State the blood parasite species.
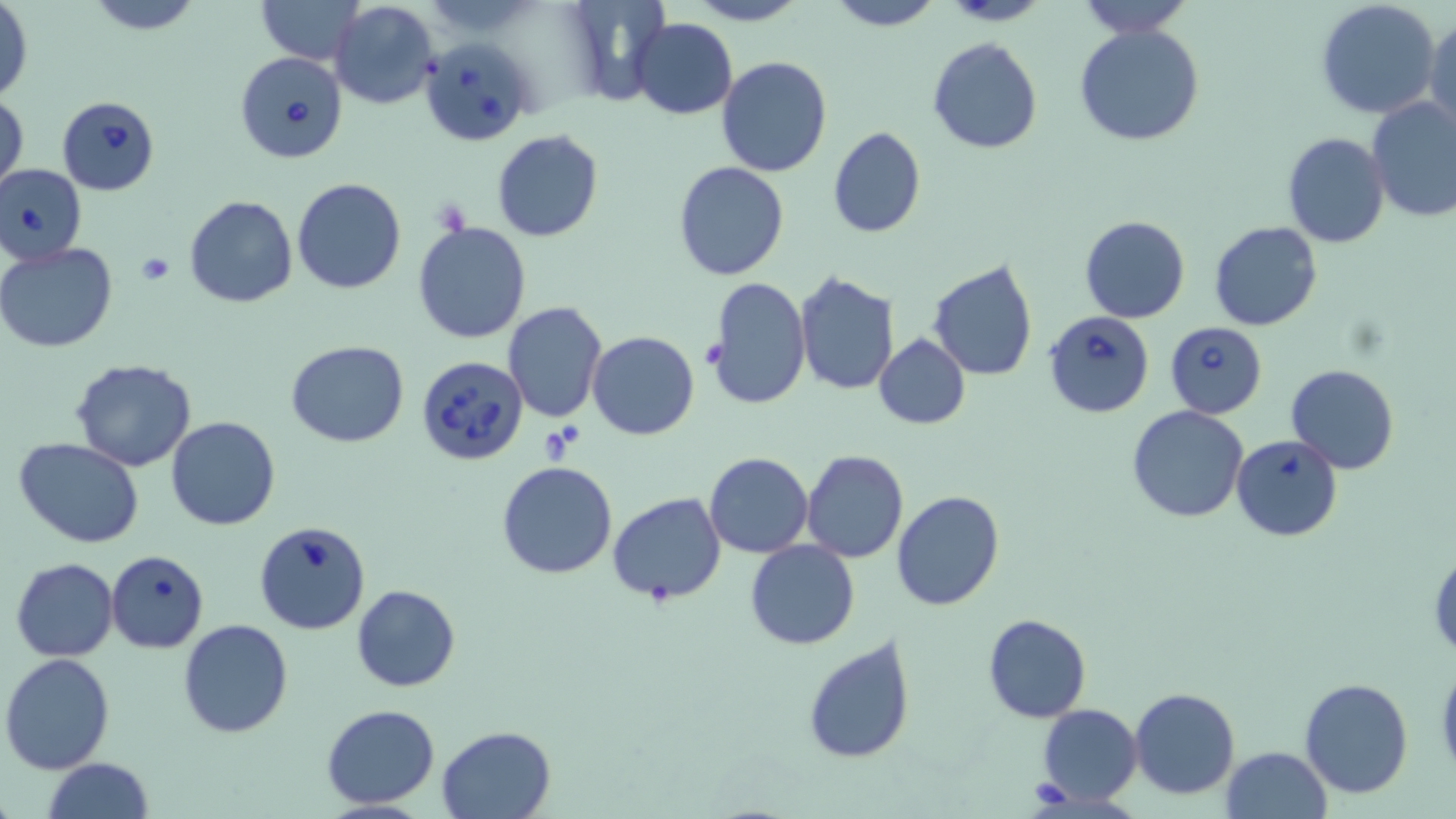
Babesia divergens.

Summary:
  - Coordinate format: approximate bounding boxes as (x1,y1)-(x2,y2) corner pairs in pixels
  - Babesia divergens-infected red blood cell locations: (420,37)-(537,145), (233,51)-(347,164), (56,95)-(162,195), (1,163)-(88,265), (1043,310)-(1155,419), (1164,321)-(1267,417), (415,356)-(528,467), (254,521)-(371,636)
  - Uninfected red blood cell locations: (257,0)-(365,64), (686,0)-(808,26), (822,0)-(944,30), (940,0)-(1049,26), (1315,0)-(1442,119), (82,1)-(206,35), (329,1)-(441,110), (1076,1)-(1195,38), (1,3)-(33,104), (1424,15)-(1455,133), (631,18)-(738,119), (1074,23)-(1207,148), (928,37)-(1042,154), (716,55)-(833,176), (1,91)-(27,197), (1366,98)-(1455,223), (828,126)-(926,238), (492,130)-(605,243), (1282,132)-(1389,249), (674,160)-(789,281), (292,177)-(407,294), (184,195)-(298,308), (1080,215)-(1190,324), (1208,221)-(1323,331), (412,222)-(532,344), (0,244)-(117,353), (929,259)-(1038,381), (794,272)-(898,393), (706,276)-(810,412), (501,300)-(607,423), (586,331)-(699,440), (875,333)-(970,429), (286,341)-(411,448), (70,359)-(197,472), (1287,364)-(1398,475), (1126,405)-(1249,524), (167,416)-(279,531), (1232,434)-(1343,541), (15,438)-(146,549), (801,449)-(909,562), (704,452)-(814,558), (497,461)-(618,580), (892,490)-(1006,611), (607,491)-(726,605), (745,541)-(859,649), (1428,543)-(1456,658), (107,549)-(210,653), (11,557)-(119,662), (351,584)-(460,692), (982,613)-(1092,723), (177,619)-(295,738), (803,634)-(916,764), (1,653)-(118,774), (1435,659)-(1456,776), (1299,678)-(1414,800), (1129,687)-(1241,799), (322,704)-(440,810), (1036,704)-(1142,804), (436,724)-(556,819), (1221,746)-(1332,819), (42,758)-(154,819)
  - Platelet locations: (138,253)-(175,286), (1024,779)-(1075,812)
  - Field of view: one of a larger specimen
  - Stain: May-Grünwald-Giemsa
  - Magnification: 1000x
  - Image size: 1456×819 pixels
  - Preparation: thin blood film
  - Modality: optical microscopy